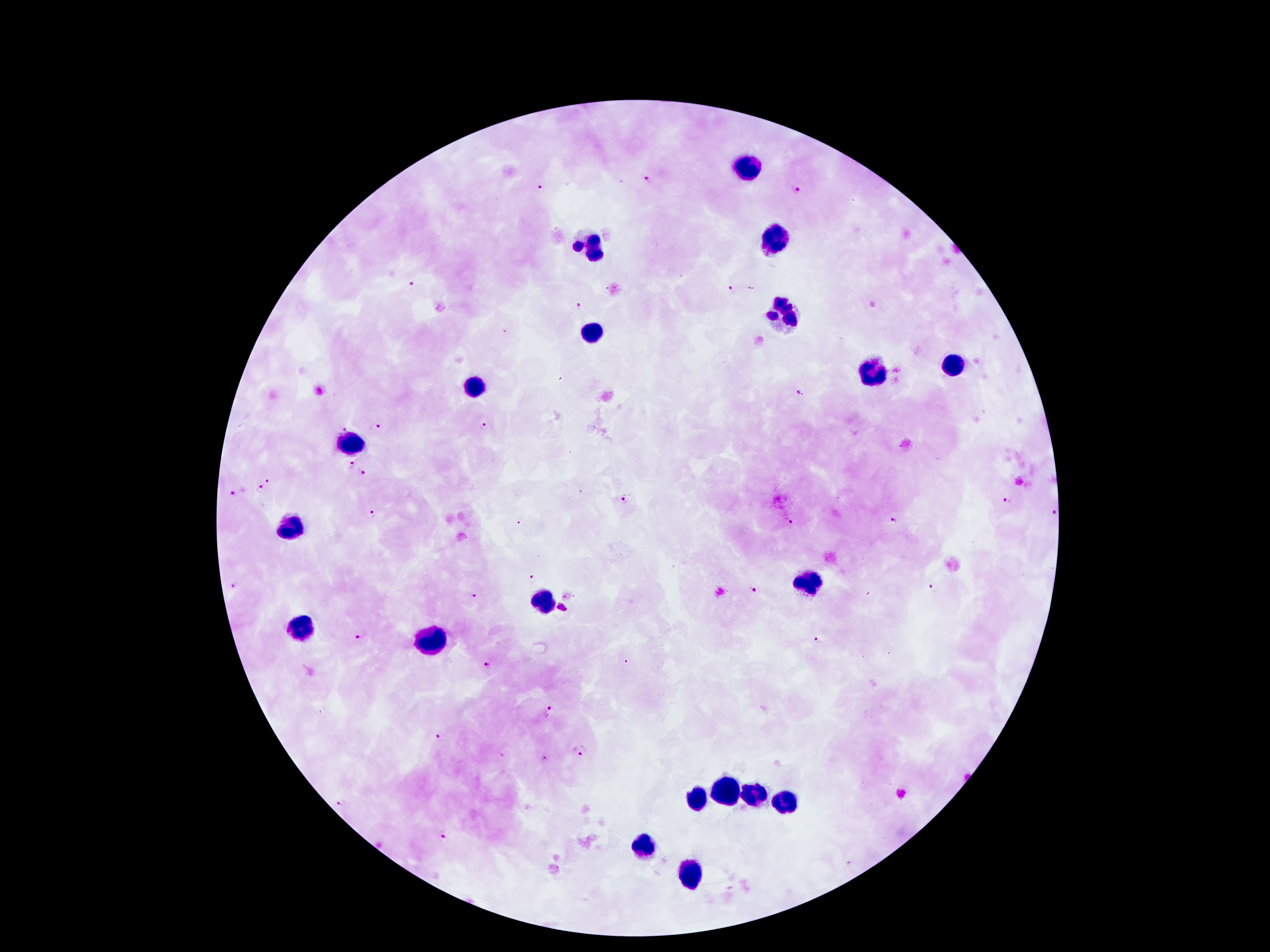

coordinate format = approximate centers as (x, y) in pixels
malaria parasite locations = (650, 177), (797, 189), (544, 190), (410, 281), (732, 289), (578, 305), (797, 393), (342, 425), (376, 425), (486, 425), (348, 463), (364, 473), (268, 479), (261, 488), (235, 492), (625, 499), (1008, 501), (368, 513), (1052, 513), (791, 521), (891, 521), (521, 524), (533, 573), (232, 586), (753, 588), (934, 588), (475, 595), (562, 606), (363, 635), (819, 638), (490, 661), (548, 713), (441, 736), (580, 753), (547, 761), (344, 803), (445, 832)
leukocyte locations = (748, 170), (778, 240), (594, 247), (785, 317), (591, 335), (955, 365), (871, 373), (472, 386), (353, 445), (293, 524), (808, 583), (545, 599), (297, 624), (435, 638), (729, 787), (757, 794), (696, 799), (787, 799), (645, 845), (689, 873)
field of view = one from this slide
stain = Giemsa
capture = smartphone through the microscope eyepiece
patient malaria status = positive for Plasmodium falciparum
preparation = thick blood smear
magnification = 100x
image size = 1270×952 pixels